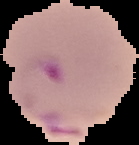

image type = cell region segmented out of the field of view; surrounding area masked to black
image size = 139×145 pixels
preparation = thin blood smear
malaria status = parasitized